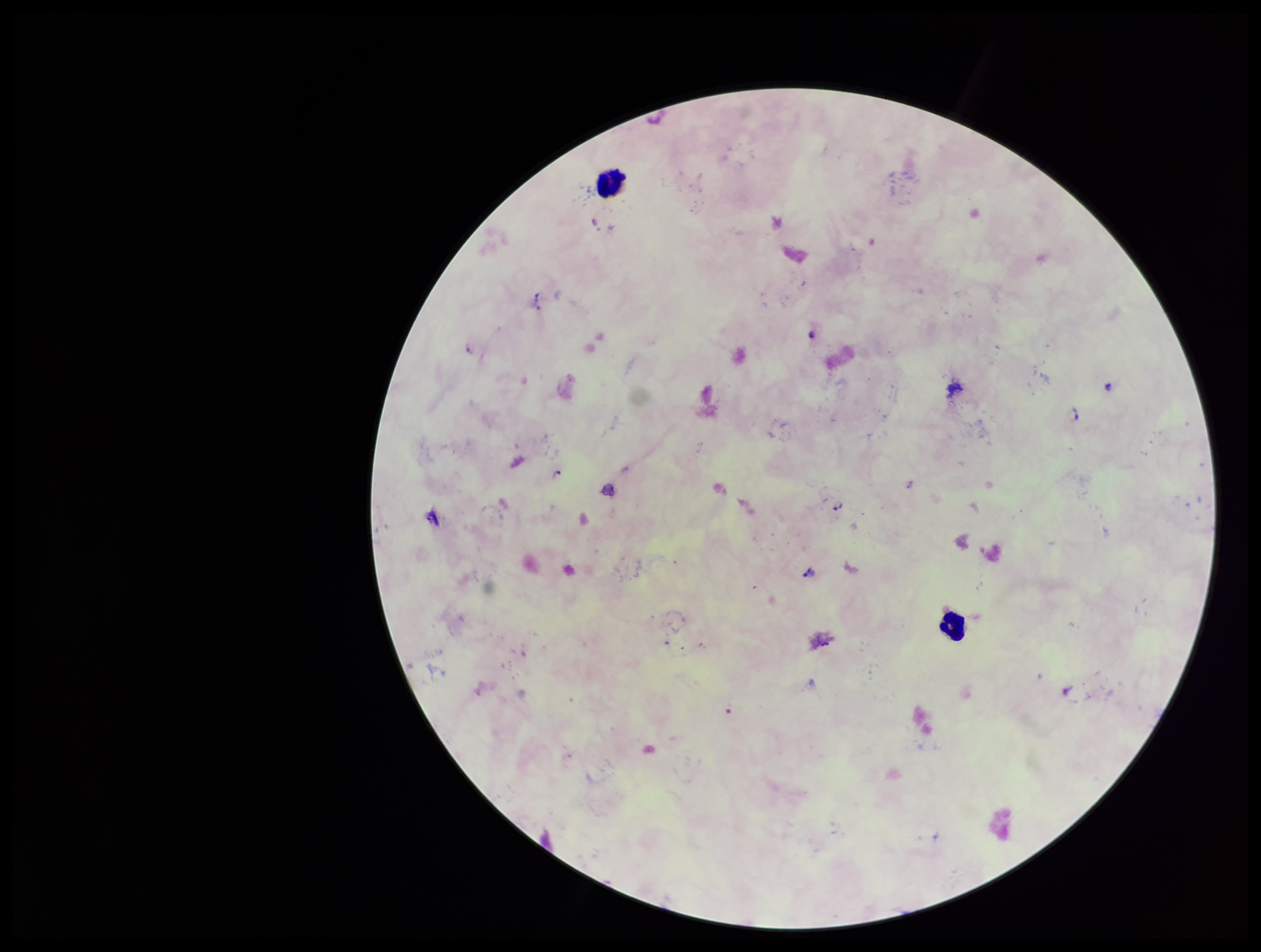 Parasite count: 5. Leukocyte count: 2. Patient malaria status: positive. Image is 1261×952 pixels. Preparation: thick. Species reported for this patient: Plasmodium falciparum. One field from this slide. Plasmodium parasites: identified. Smartphone photograph taken through the eyepiece of a microscope. Stained with Giemsa.